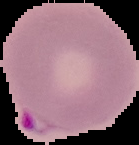
result = Plasmodium parasites identified
preparation = thin blood film
image size = 139×145 pixels
image type = segmented cell region with the area outside set to black